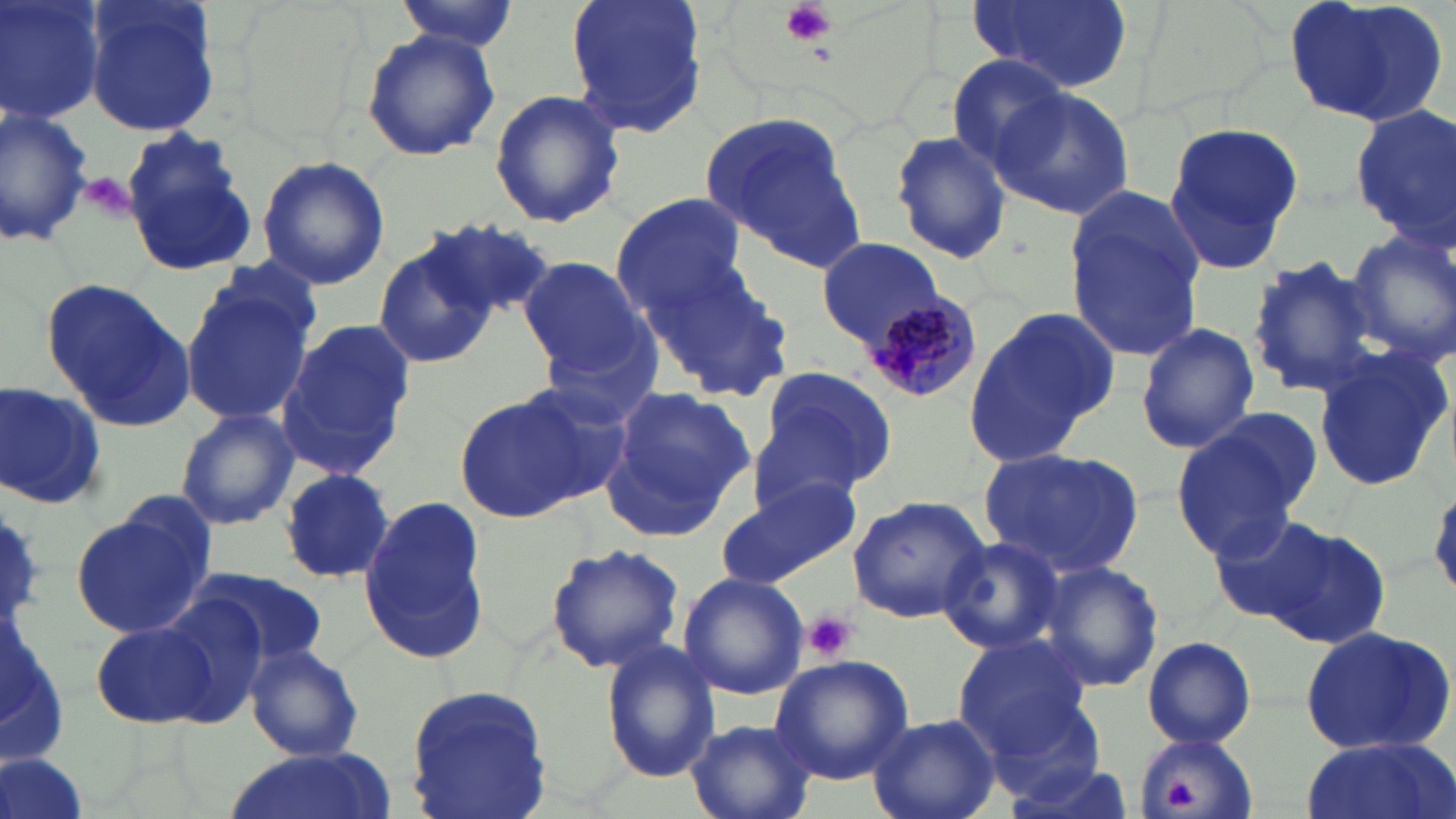

Summary:
  - Coordinate format: approximate bounding boxes as [x1, y1, x2, y2] in pixels
  - Uninfected red blood cell locations: [1, 0, 106, 126], [82, 0, 222, 139], [566, 0, 708, 140], [964, 0, 1133, 96], [1280, 0, 1453, 127], [391, 1, 519, 55], [361, 27, 499, 162], [945, 56, 1071, 175], [991, 87, 1137, 219], [488, 89, 625, 230], [0, 103, 98, 252], [1348, 103, 1456, 244], [696, 110, 866, 270], [1162, 126, 1306, 273], [889, 128, 1014, 267], [121, 131, 257, 276], [256, 158, 390, 289], [1061, 187, 1206, 363], [610, 192, 746, 317], [426, 221, 553, 325], [1343, 228, 1456, 368], [371, 237, 494, 365], [815, 237, 944, 348], [642, 255, 793, 402], [518, 257, 651, 378], [1247, 257, 1386, 398], [181, 272, 318, 433], [43, 278, 193, 432], [962, 307, 1116, 471], [1135, 318, 1259, 454], [278, 320, 412, 477], [1313, 344, 1451, 493], [752, 367, 896, 499], [2, 383, 108, 509], [603, 386, 755, 538], [455, 392, 593, 523], [174, 408, 299, 531], [1170, 411, 1313, 555], [979, 446, 1146, 574], [277, 468, 395, 585], [717, 472, 860, 589], [847, 493, 990, 623], [359, 495, 493, 663], [71, 498, 217, 641], [1205, 510, 1335, 628], [1259, 520, 1395, 647], [938, 537, 1066, 656], [545, 542, 685, 673], [1038, 561, 1164, 692], [187, 566, 331, 669], [678, 571, 809, 701], [151, 593, 272, 722], [88, 616, 222, 732], [1298, 623, 1456, 758], [952, 631, 1095, 758], [1141, 634, 1256, 748], [600, 639, 721, 782], [242, 643, 365, 761], [770, 655, 913, 786], [404, 683, 554, 819], [868, 714, 1000, 819], [685, 719, 820, 819], [1132, 731, 1259, 819], [1298, 737, 1452, 819], [230, 749, 384, 819], [1, 752, 89, 819]
  - Platelet locations: [779, 0, 837, 47], [802, 611, 858, 663], [1164, 780, 1196, 808]
  - Plasmodium malariae-infected red blood cell locations: [861, 297, 977, 406]
  - Slide-level diagnosis: Plasmodium malariae
  - Magnification: 1000x
  - Field of view: single
  - Modality: light microscopy
  - Preparation: thin blood film
  - Stain: May-Grünwald-Giemsa
  - Image size: 1456×819 pixels